Classify the preparation.
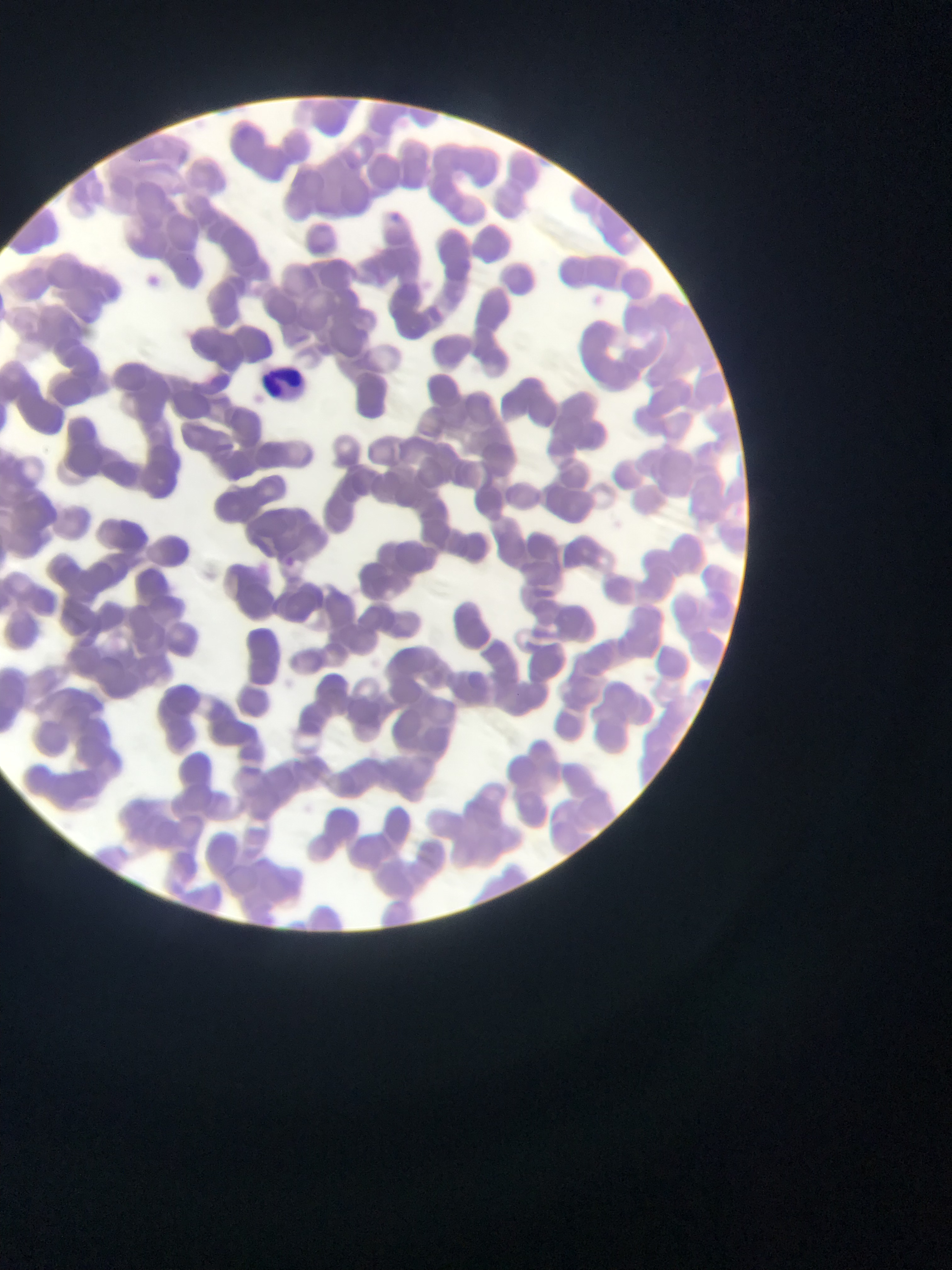
Thin blood film.

Approximate bounding boxes as left top right bottom in pixels.
Summary:
  - Malaria parasite locations: 279 553 299 573
  - Leukocyte locations: 262 359 317 406
  - Field of view: single
  - Capture: mobile-phone photograph through a microscope
  - Country: Ghana
  - Image size: 952×1270 pixels